Assess this cell for malaria.
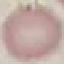
Uninfected.

capture: smartphone camera at the microscope eyepiece
preparation: thin blood film
image_type: automatically extracted cell patch, resized to 64 × 64 pixels
stain: Giemsa